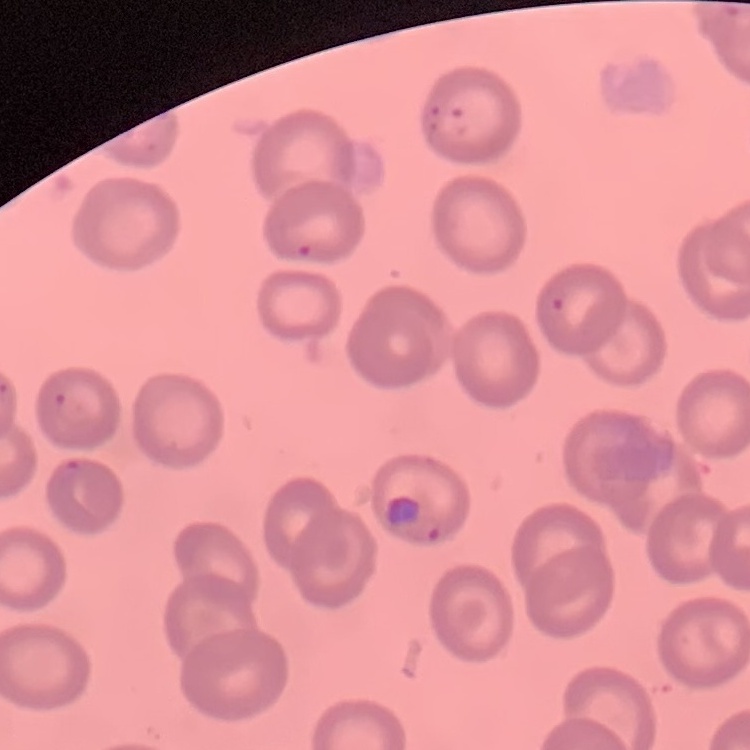
Summary:
  - Erythrocyte morphology: no rouleaux formation
  - Image type: square crop of a larger photomicrograph
  - Preparation: thin blood smear
  - Stain: Field's or Giemsa